Give the extent of all Plasmodium vivax-infected red blood cells.
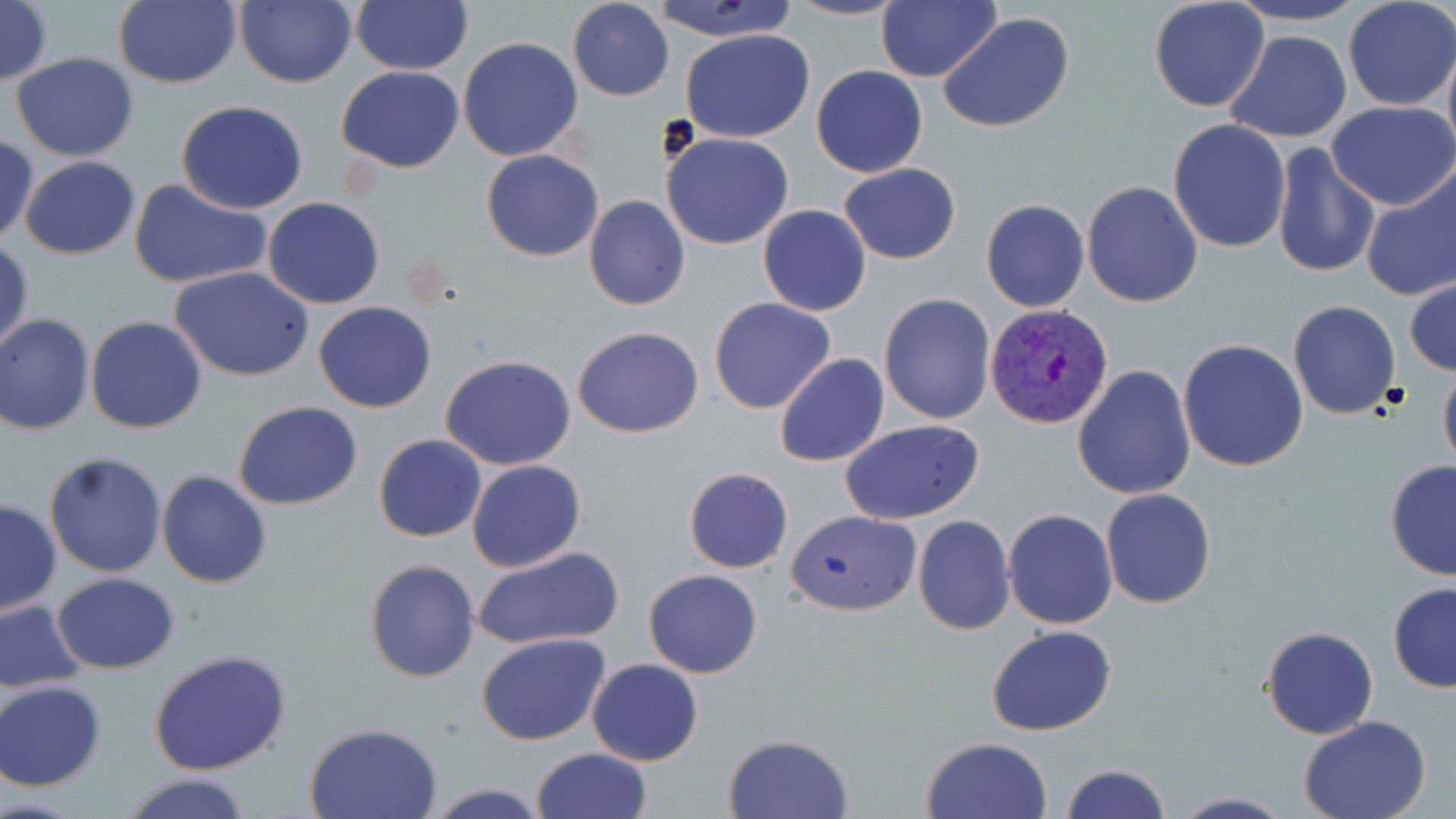

Approximate bounding boxes as (x1,y1)-(x2,y2) corner pairs in pixels.
Plasmodium vivax-infected red blood cells: (985,304)-(1114,430).

Uninfected red blood cell locations: (0,0)-(51,87), (112,0)-(241,89), (234,0)-(357,87), (647,0)-(804,43), (785,0)-(908,21), (877,0)-(1000,83), (1148,0)-(1269,112), (1222,0)-(1373,27), (350,1)-(472,76), (569,1)-(674,101), (1342,1)-(1455,111), (938,13)-(1076,133), (681,28)-(814,143), (1223,30)-(1352,143), (458,37)-(584,161), (1442,39)-(1456,166), (10,53)-(140,162), (811,65)-(928,178), (337,67)-(463,171), (175,100)-(307,215), (1327,101)-(1456,211), (1278,118)-(1437,253), (1168,120)-(1291,252), (661,130)-(793,250), (1,133)-(38,246), (1271,145)-(1381,279), (480,149)-(604,262), (19,156)-(140,258), (838,163)-(961,266), (1359,165)-(1456,305), (130,180)-(271,289), (1082,181)-(1203,306), (584,195)-(691,310), (262,197)-(384,309), (981,198)-(1089,313), (757,205)-(871,316), (1,236)-(33,355), (171,267)-(315,382), (1405,275)-(1455,377), (879,294)-(997,425), (709,298)-(836,416), (1288,299)-(1401,420), (314,302)-(436,413), (1,314)-(94,435), (85,315)-(207,432), (573,326)-(703,438), (1178,340)-(1308,470), (441,354)-(579,470), (774,354)-(889,469), (1073,364)-(1197,502), (1438,365)-(1456,478), (234,400)-(363,510), (839,418)-(985,525), (374,434)-(486,542), (42,451)-(167,578), (466,460)-(586,572), (1384,460)-(1456,580), (685,467)-(793,573), (156,471)-(271,588), (1100,487)-(1215,608), (0,499)-(62,617), (1003,508)-(1117,629), (788,509)-(922,616), (912,515)-(1015,635), (471,546)-(624,651), (363,558)-(481,682), (643,569)-(763,677), (53,573)-(179,672), (1387,582)-(1456,692), (0,598)-(87,696), (986,625)-(1116,736), (1262,626)-(1378,740), (477,633)-(610,746), (149,649)-(293,775), (587,659)-(703,766), (0,681)-(106,790), (1299,715)-(1430,819), (304,722)-(444,818), (722,733)-(852,818), (921,736)-(1054,819), (532,747)-(653,819), (1059,763)-(1170,819), (120,772)-(254,819), (422,783)-(551,818), (1170,793)-(1296,819). Slide-level diagnosis: Plasmodium vivax. 1000x magnification. One field of a larger specimen. Image is 1456×819 pixels. Thin blood smear. May-Grünwald-Giemsa-stained preparation. Light microscopy.